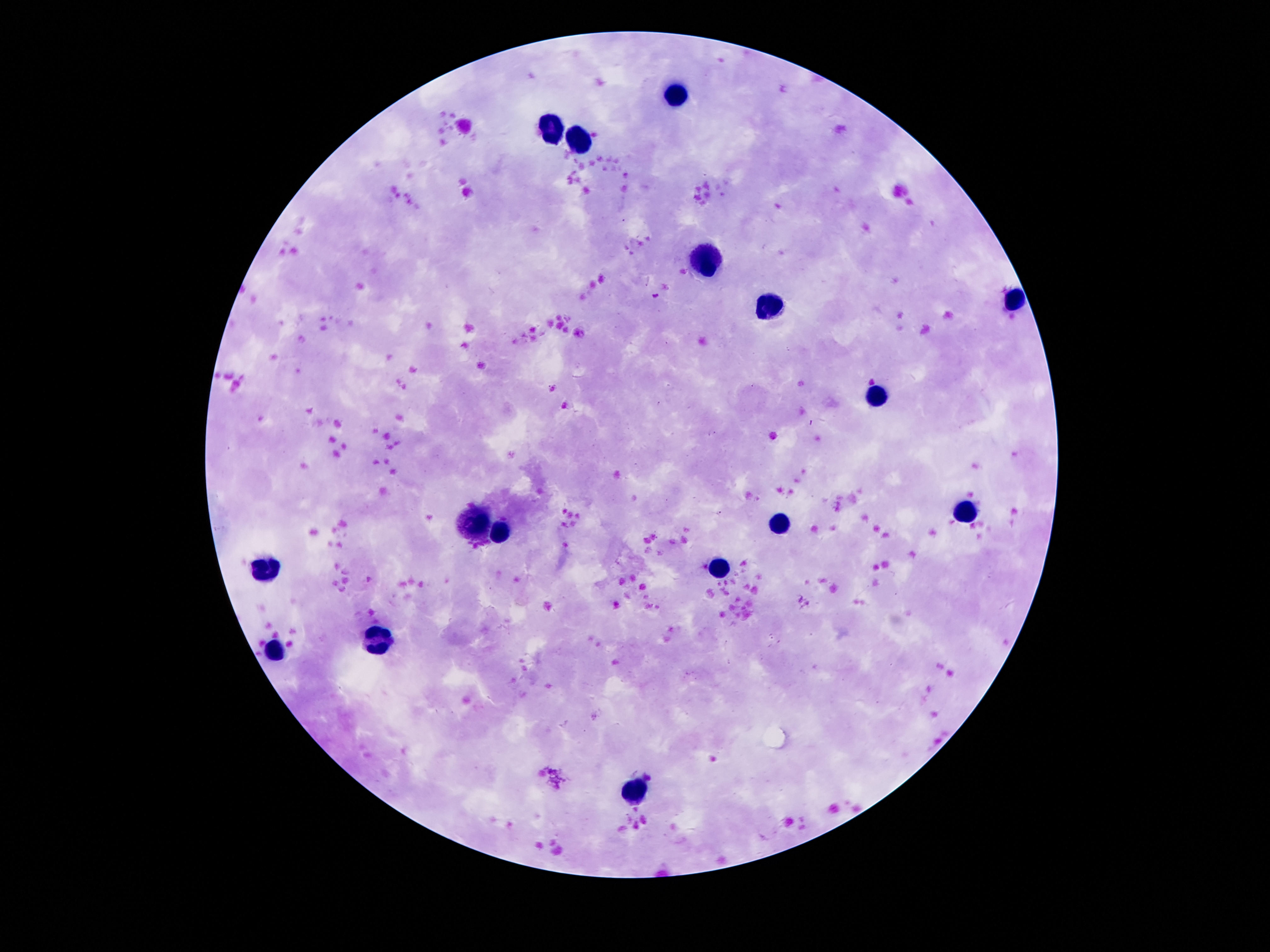

{
  "patient_malaria_status": "not infected",
  "image_size": "1270×952 pixels",
  "field_of_view": "one from this slide",
  "preparation": "thick blood smear",
  "capture": "smartphone camera through the microscope eyepiece",
  "stain": "Giemsa",
  "leukocyte_locations": "approximate centers as {x, y} in pixels: {672, 95}, {552, 126}, {581, 138}, {704, 263}, {1016, 299}, {764, 306}, {879, 390}, {968, 510}, {780, 522}, {475, 527}, {502, 532}, {269, 568}, {718, 568}, {375, 640}, {271, 652}, {632, 789}",
  "magnification": "100x"
}